Outline each blood parasite and name the species.
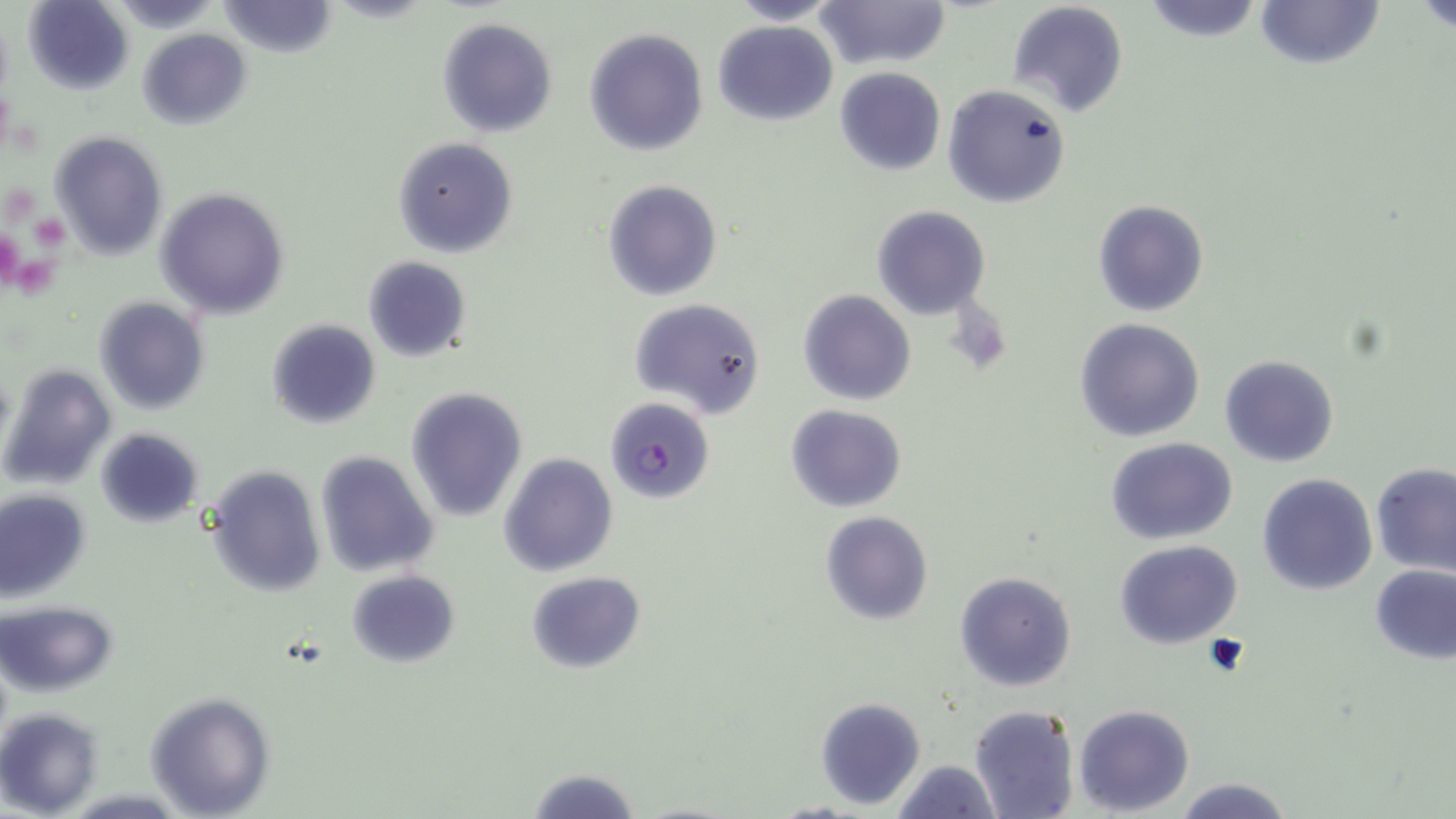

Approximate bounding boxes as [x1, y1, x2, y2] in pixels.
Plasmodium falciparum-infected red blood cells: [604, 397, 715, 504].
No Plasmodium ovale, Plasmodium malariae, Plasmodium vivax, Babesia divergens, or Trypanosoma brucei observed.

Summary:
  - Platelet locations: [29, 212, 72, 252], [0, 232, 25, 291], [16, 253, 56, 299]
  - Uninfected red blood cell locations: [815, 0, 948, 70], [1140, 0, 1266, 43], [1252, 0, 1385, 71], [1416, 0, 1456, 35], [25, 1, 135, 92], [216, 1, 338, 57], [727, 1, 842, 24], [1005, 1, 1129, 117], [437, 18, 557, 138], [713, 18, 838, 125], [583, 28, 708, 155], [138, 29, 250, 128], [833, 67, 945, 176], [942, 84, 1071, 209], [51, 131, 166, 259], [394, 136, 518, 258], [603, 181, 722, 301], [155, 187, 291, 320], [1092, 199, 1211, 318], [871, 206, 991, 320], [362, 256, 472, 362], [798, 289, 918, 406], [94, 297, 209, 417], [630, 298, 766, 421], [1074, 317, 1205, 442], [266, 319, 380, 429], [1219, 353, 1340, 467], [1, 363, 116, 490], [405, 387, 528, 522], [786, 405, 908, 512], [96, 429, 203, 526], [1105, 436, 1239, 544], [314, 451, 439, 576], [498, 453, 619, 576], [204, 465, 326, 597], [1372, 465, 1456, 576], [1258, 473, 1378, 594], [1, 489, 90, 601], [821, 511, 933, 627], [1115, 540, 1243, 649], [1370, 565, 1455, 662], [347, 569, 461, 668], [954, 569, 1078, 692], [527, 572, 645, 674], [2, 601, 118, 697], [143, 691, 274, 817], [814, 696, 925, 810], [970, 704, 1082, 819], [1075, 704, 1194, 815], [1, 707, 104, 816], [892, 759, 1001, 819], [528, 766, 639, 819], [1172, 775, 1294, 818]
  - Slide-level diagnosis: Plasmodium falciparum
  - Image size: 1456×819 pixels
  - Stain: May-Grünwald-Giemsa
  - Field of view: one of a larger specimen
  - Modality: light microscopy
  - Magnification: 1000x
  - Preparation: thin blood film